Report the malaria status of this cell.
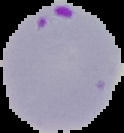
It is parasitized.

image type = segmented cell region on a black background
preparation = thin blood film
image size = 124×133 pixels